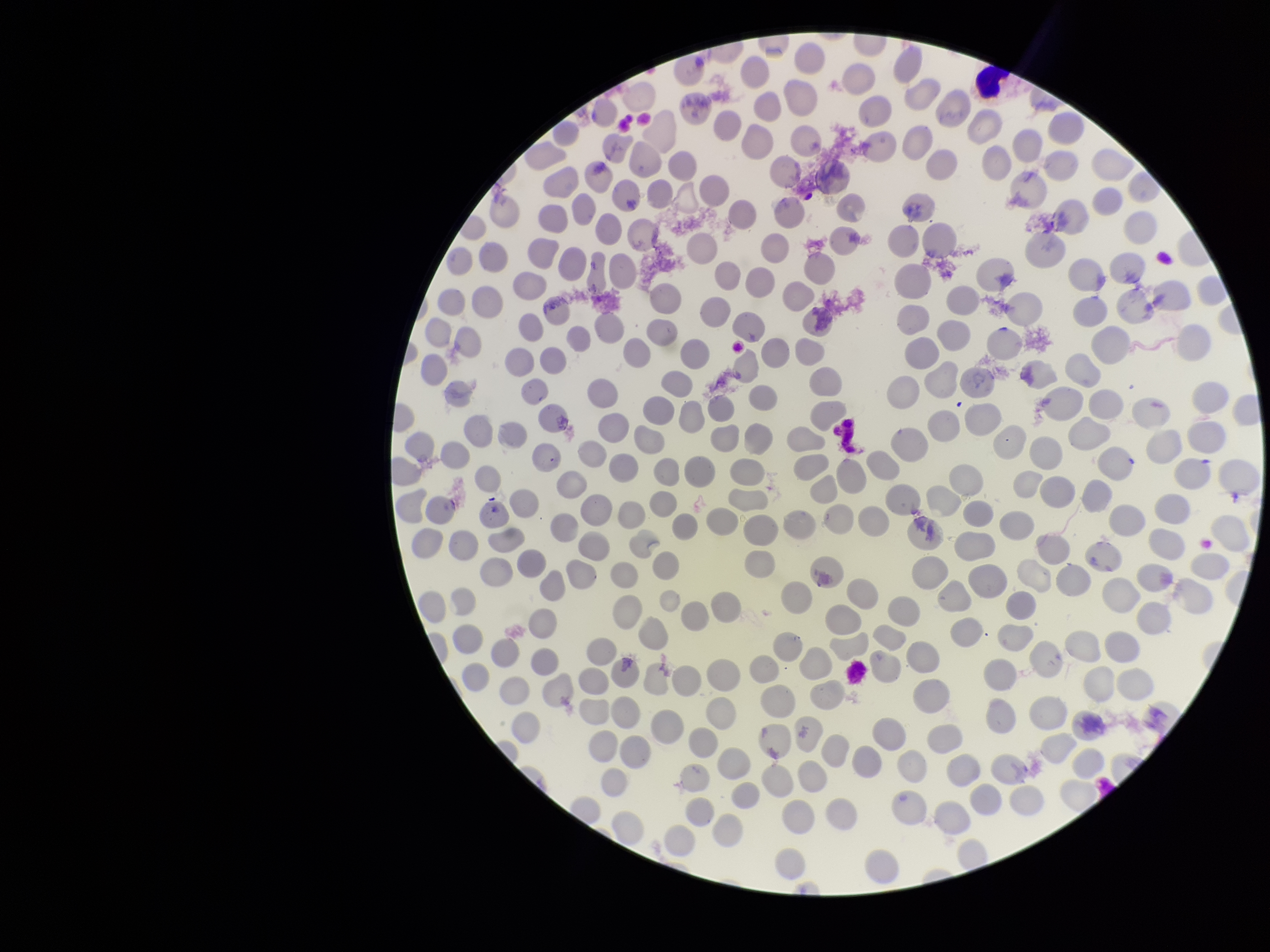

capture: smartphone photograph through the microscope eyepiece
red_blood_cell_count: 295
parasitized_red_blood_cell_count: 0
parasitized_red_blood_cells: none seen
image_size: 1270×952 pixels
stain: Giemsa
preparation: thin
field_of_view: one from this slide
patient_malaria_status: negative